Describe the morphology of the red blood cells.
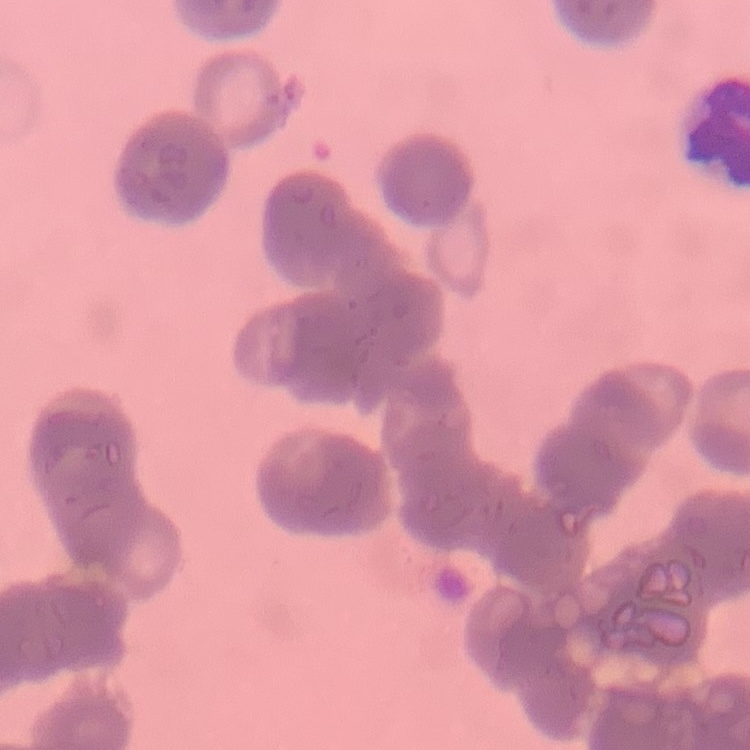

Rouleaux formation.

Summary:
  - Preparation: thin peripheral smear
  - Image type: square crop of a larger photomicrograph
  - Stain: Field's or Giemsa